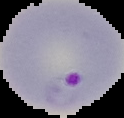
image size = 124×118 pixels
preparation = thin blood smear
image type = segmented cell region with the area outside set to black
result = malaria parasites detected